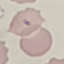
Summary:
  - Result: no malaria parasites detected
  - Capture: smartphone through the microscope eyepiece
  - Stain: Giemsa
  - Image type: cell patch, automatically extracted from a larger field of view and resized to 64 × 64 pixels
  - Preparation: thin blood smear